Report the malaria status of this cell.
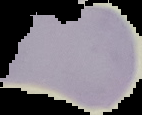

It is uninfected.

Image is 142×115 pixels. From a thin blood smear. Cell region segmented out of the field of view; the surrounding area is masked to black.